Report the malaria status of this cell.
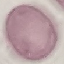

It is uninfected.

capture: smartphone camera at the microscope eyepiece
preparation: thin blood smear
image_type: automatically extracted cell patch, resized to 64 × 64 pixels
stain: Giemsa